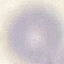

Result: no malaria parasites detected. Thin blood smear. Automatically extracted cell patch, resized to 64 × 64 pixels. Giemsa stain. Photographed with a smartphone camera at the microscope eyepiece.